Name the blood parasite species.
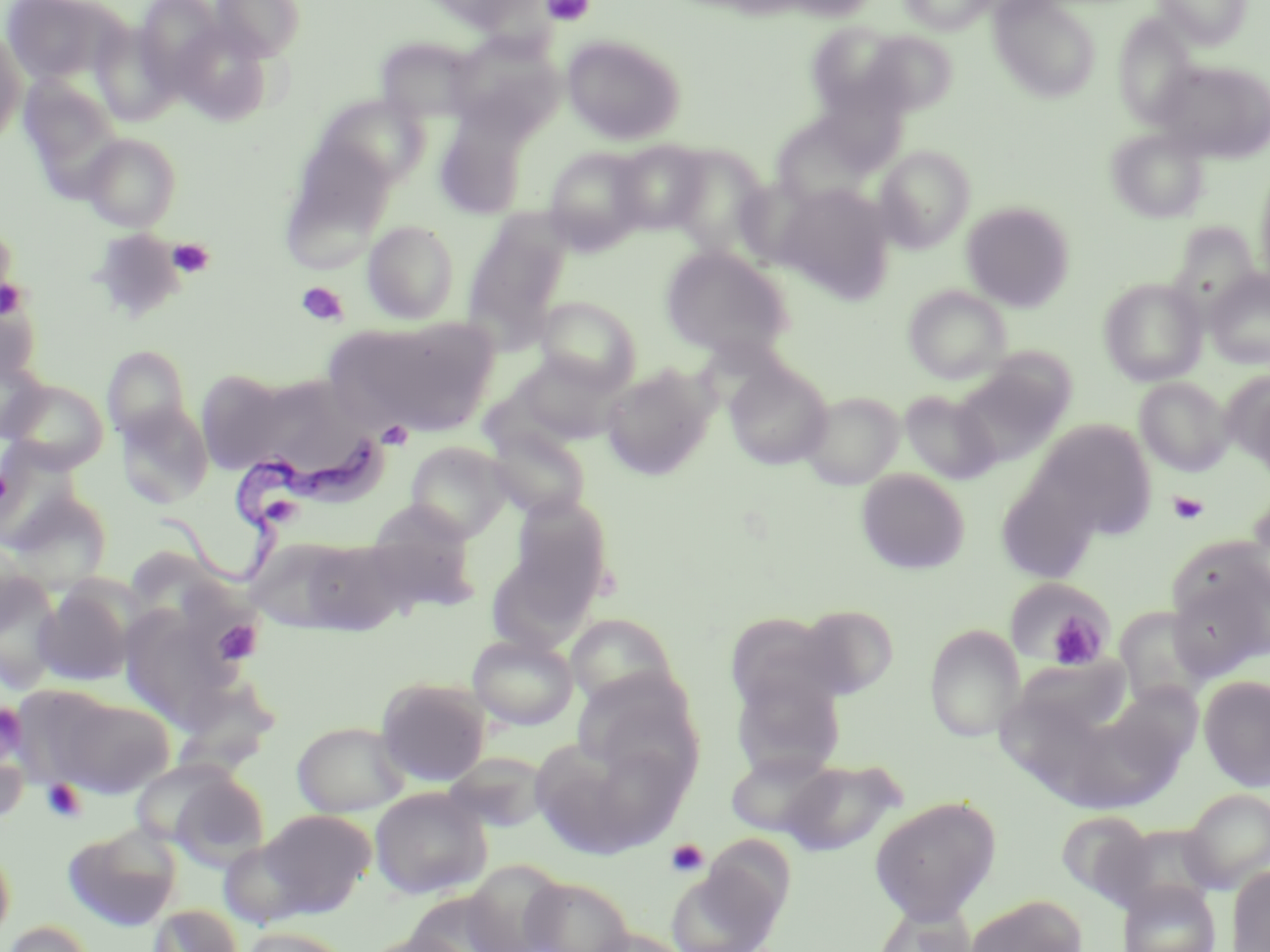

Trypanosoma brucei.

Approximate bounding boxes as (x1,y1)-(x2,y2) corner pairs in pixels. Uninfected red blood cell locations (subset): (0,0)-(130,88), (134,0)-(230,92), (210,0)-(307,61), (418,0)-(545,34), (774,0)-(884,21), (899,0)-(997,34), (988,0)-(1102,102), (1153,0)-(1252,49), (1112,14)-(1199,128), (169,20)-(276,125), (807,21)-(912,120), (0,29)-(25,146), (857,30)-(960,116), (444,32)-(562,139), (562,34)-(686,145), (376,36)-(485,124), (1152,58)-(1270,163), (18,74)-(122,190), (314,93)-(430,191), (434,110)-(529,219), (769,110)-(886,212), (1107,128)-(1210,224), (81,133)-(181,231), (278,138)-(396,270), (611,140)-(710,232), (874,145)-(975,252), (665,146)-(773,256), (544,147)-(650,253), (1255,165)-(1270,291), (774,184)-(896,302), (961,201)-(1076,311), (463,213)-(572,349), (363,220)-(459,325), (1168,223)-(1262,317), (661,246)-(794,360), (1204,269)-(1270,370), (1099,277)-(1208,386), (903,285)-(1011,384), (0,292)-(43,388), (535,296)-(641,393), (334,316)-(499,435), (102,345)-(191,442), (0,349)-(50,444), (508,351)-(624,445), (955,356)-(1075,464), (724,360)-(833,471), (600,364)-(716,480), (195,370)-(292,472), (1223,371)-(1270,474), (246,373)-(379,489), (1134,377)-(1233,476), (2,378)-(110,472), (900,389)-(1000,484), (800,391)-(904,490), (115,402)-(213,508), (1034,420)-(1157,539), (484,423)-(592,521), (405,442)-(512,542), (995,466)-(1104,584), (856,468)-(970,575), (3,485)-(113,592), (1245,492)-(1270,602), (503,493)-(615,615), (360,506)-(481,612), (261,535)-(416,636), (0,541)-(45,640), (1167,559)-(1268,680), (1,568)-(63,688), (34,582)-(138,686), (1012,582)-(1115,671), (119,601)-(247,727), (795,603)-(900,700), (1113,607)-(1214,710), (724,611)-(850,720), (565,613)-(680,711), (924,624)-(1024,743), (467,633)-(578,731), (1007,655)-(1134,745), (730,671)-(847,780), (572,672)-(705,790), (1198,675)-(1270,791), (375,677)-(492,786), (51,693)-(174,798), (1053,700)-(1183,813), (0,712)-(31,824), (292,721)-(411,818), (532,732)-(685,856), (724,749)-(838,837), (442,752)-(550,831), (779,758)-(904,856), (152,765)-(270,866), (369,787)-(493,899), (1182,789)-(1270,893), (869,796)-(1001,924), (255,809)-(377,915), (1056,810)-(1154,905), (1108,823)-(1221,917), (63,824)-(182,931), (0,840)-(15,944), (666,861)-(785,952), (1227,864)-(1270,952), (520,876)-(635,952), (1118,879)-(1221,952), (966,894)-(1086,952), (872,902)-(979,952), (148,904)-(243,952), (1,921)-(96,952), (239,926)-(356,952), (583,928)-(693,952), (359,932)-(476,952). Trypanosoma brucei locations: (154,438)-(381,597). Platelet locations (subset): (542,0)-(595,26), (167,238)-(215,278), (0,276)-(27,322), (296,281)-(348,325), (377,421)-(413,449), (1168,491)-(1209,525), (1043,606)-(1111,670), (213,620)-(263,665), (0,701)-(27,759), (41,779)-(87,823), (665,838)-(709,878). Captured at 1000x magnification. Light microscopy. May-Grünwald-Giemsa stain. Image is 1270×952 pixels. Thin blood smear. One field of a larger specimen.